Outline each Plasmodium parasite.
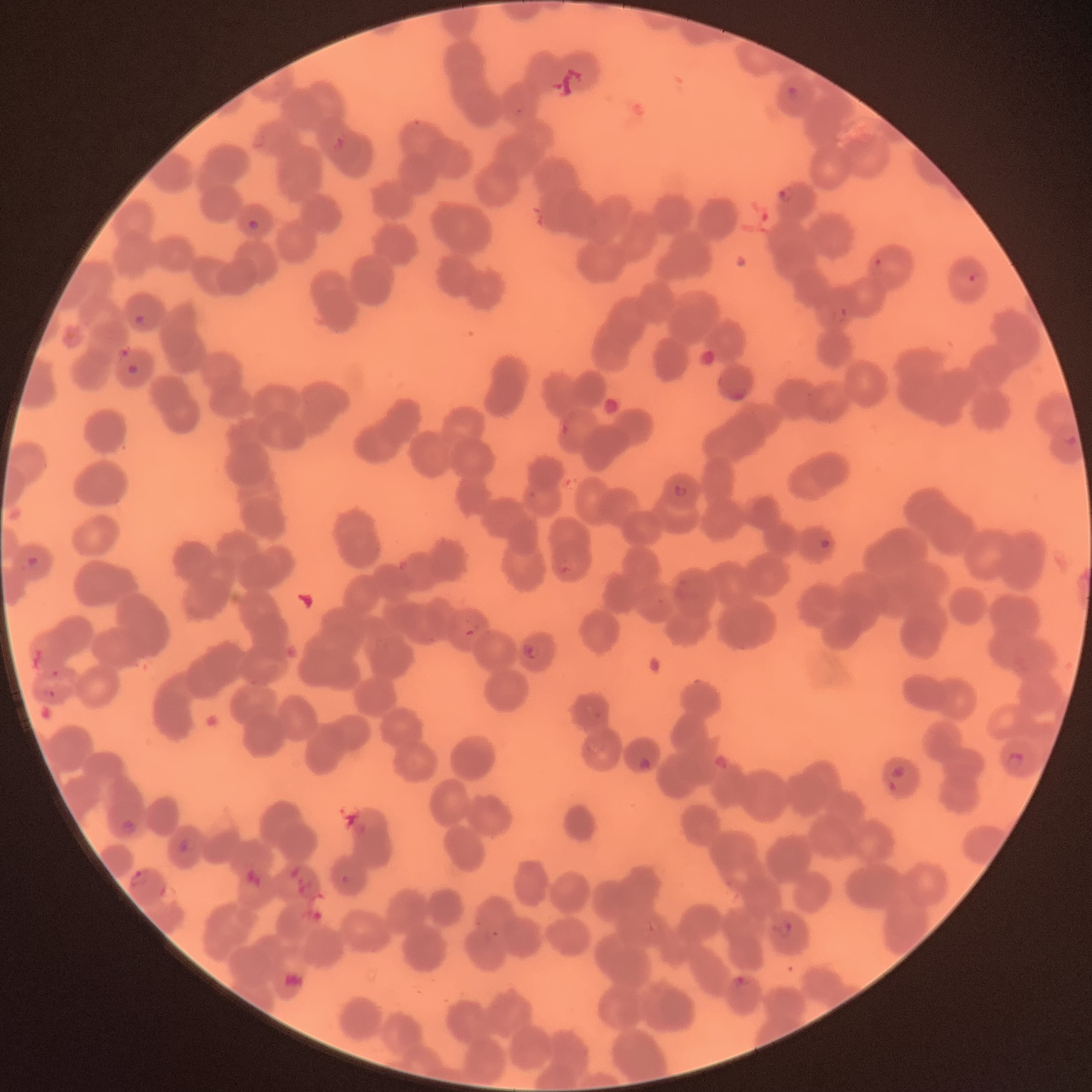

Approximate bounding boxes as [x1, y1, x2, y2] in pixels.
Plasmodium parasites: [788, 85, 800, 97], [514, 107, 525, 116], [254, 134, 265, 148], [332, 135, 347, 152], [776, 186, 795, 202], [246, 220, 261, 230], [875, 258, 883, 267], [969, 274, 982, 282], [831, 307, 849, 324], [135, 315, 146, 326], [120, 346, 131, 358], [128, 364, 139, 374], [732, 388, 746, 401], [561, 423, 572, 435], [1063, 434, 1077, 446], [673, 484, 689, 497], [527, 491, 537, 498], [821, 539, 830, 548], [25, 555, 41, 570], [560, 560, 578, 574], [397, 561, 408, 571], [657, 596, 666, 605], [462, 627, 485, 638], [374, 638, 390, 653], [524, 640, 539, 660], [52, 669, 62, 678], [250, 679, 259, 686], [44, 688, 55, 697], [586, 705, 603, 720], [585, 742, 602, 756], [1004, 752, 1025, 770], [715, 754, 729, 770], [639, 758, 651, 770], [891, 766, 906, 778], [889, 781, 897, 792], [120, 818, 136, 833], [179, 838, 189, 853], [128, 870, 149, 885], [341, 873, 353, 884], [160, 884, 166, 897], [645, 921, 659, 934], [772, 922, 793, 939], [484, 929, 500, 937], [733, 977, 745, 991].
Plasmodium parasites too small for a box (approximate centers as [x, y] in pixels): [417, 123], [432, 639], [478, 923].

The red blood cells show rouleaux formation. Thin blood film. Image is 1092×1092 pixels. Optical microscopy.